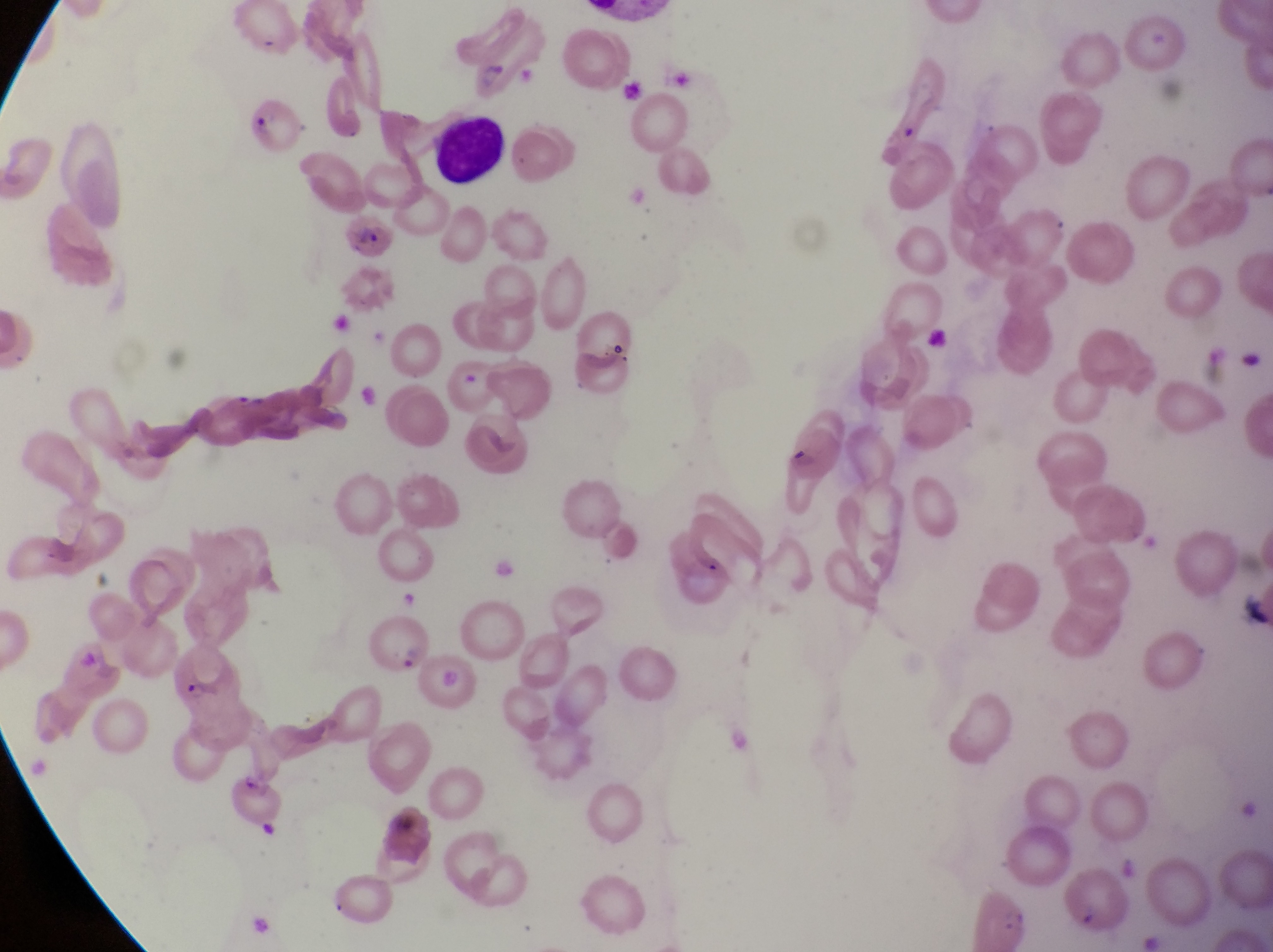

magnification = 1000x
image size = 1273×952 pixels
preparation = thin blood film
leukocyte locations = approximate bounding boxes as [left, top, right, bottom] in pixels: [435, 121, 509, 184]
country = Uganda
parasitised red blood cell locations = approximate bounding boxes as [left, top, right, bottom] in pixels: [247, 88, 305, 158], [785, 407, 848, 488], [370, 616, 430, 678], [174, 650, 252, 755], [227, 767, 280, 830]
field of view = single
capture = smartphone photograph through the eyepiece of an Olympus CX-23 microscope